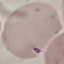
result = malaria parasites identified
preparation = thin blood film
stain = Giemsa
capture = smartphone camera at the microscope eyepiece
image type = automatically extracted cell patch, resized to 64 × 64 pixels